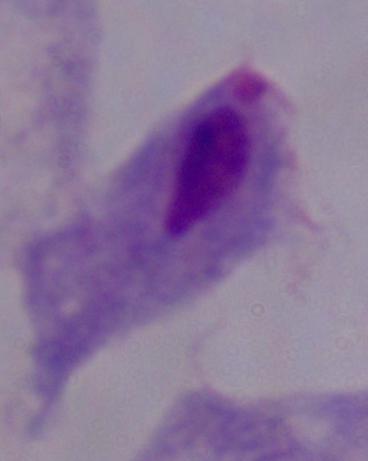

Photomicrograph. A trichomonad is seen. 1000x magnification.